Assess the morphology of the red blood cells.
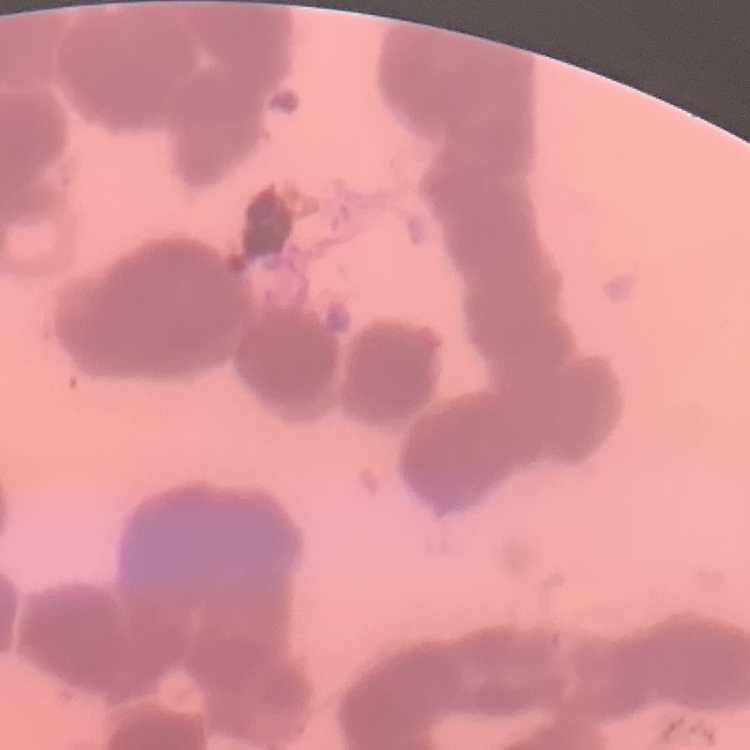

Rouleaux formation.

One tile cut from a larger photomicrograph. Field's or Giemsa stain. Thin blood film.